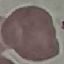

Summary:
  - Result: negative for malaria parasites
  - Stain: Giemsa
  - Image type: cell patch, automatically extracted from a larger field of view and resized to 64 × 64 pixels
  - Preparation: thin blood film
  - Capture: smartphone through the microscope eyepiece